Outline Plasmodium falciparum parasites and classify them by life-cycle stage.
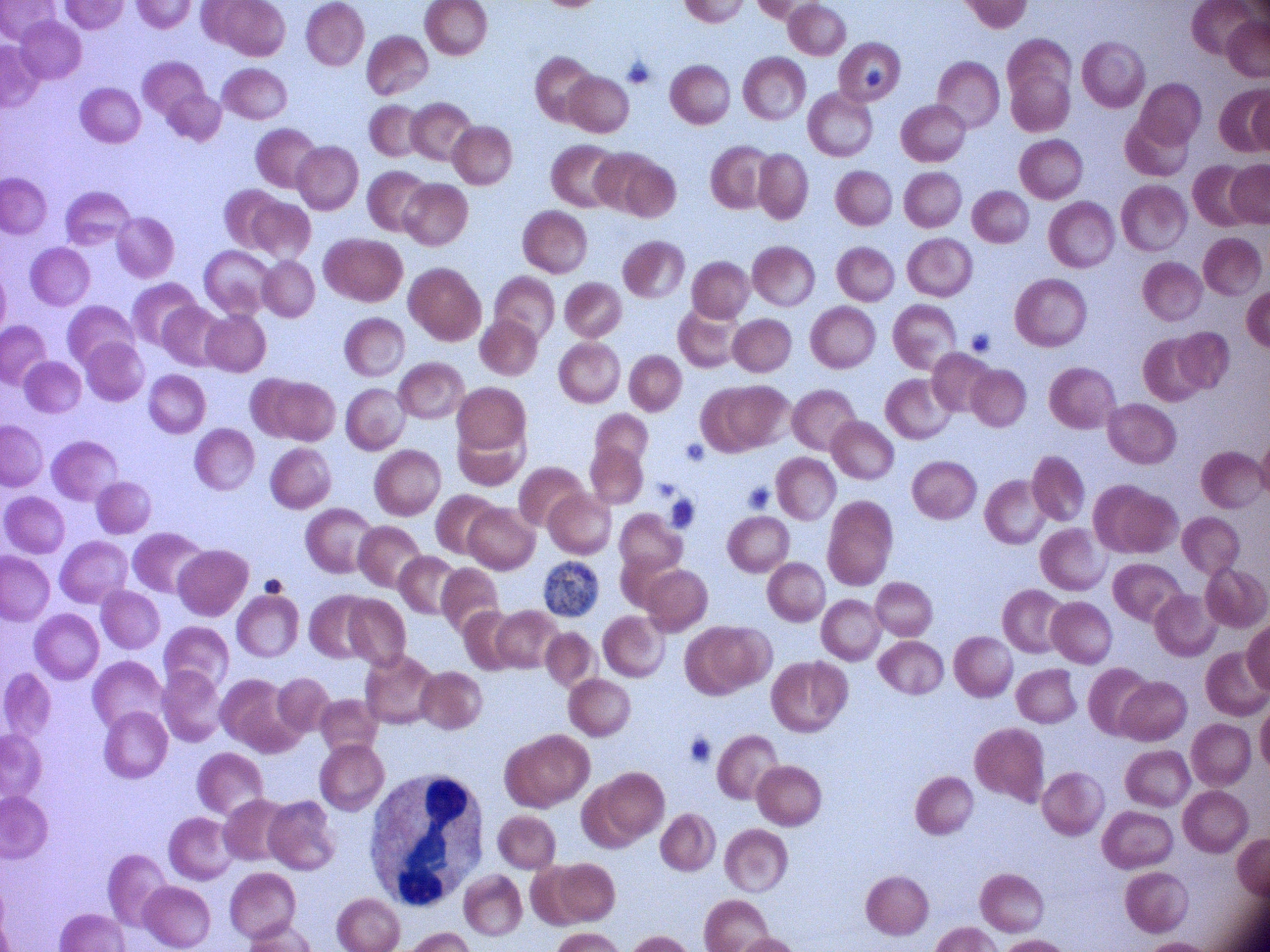
Approximate bounding boxes as (x1,y1)-(x2,y2) corner pairs in pixels, from the source annotation, which is not necessarily exhaustive.
Schizonts: (544,561)-(597,617).

Summary:
  - Stain: Giemsa
  - Microscope: Leica DM2000 with built-in camera
  - Preparation: thin blood film
  - Image size: 1270×952 pixels
  - Magnification: 100x
  - Species: Plasmodium falciparum
  - Field of view: single